Describe the morphology of the red blood cells.
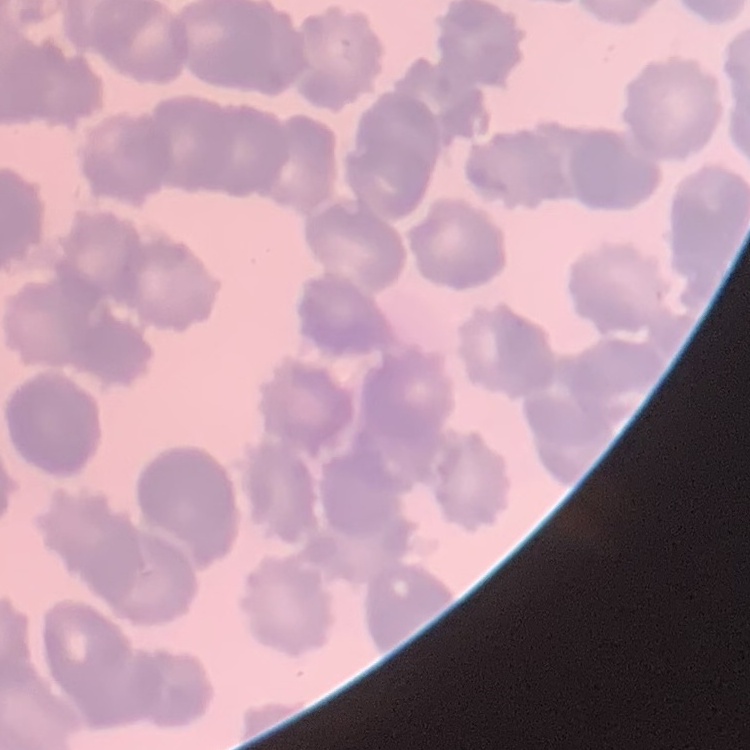

Rouleaux formation.

stain = Field's or Giemsa
image type = one tile cut from a larger photomicrograph
preparation = thin blood film